State the blood parasite species.
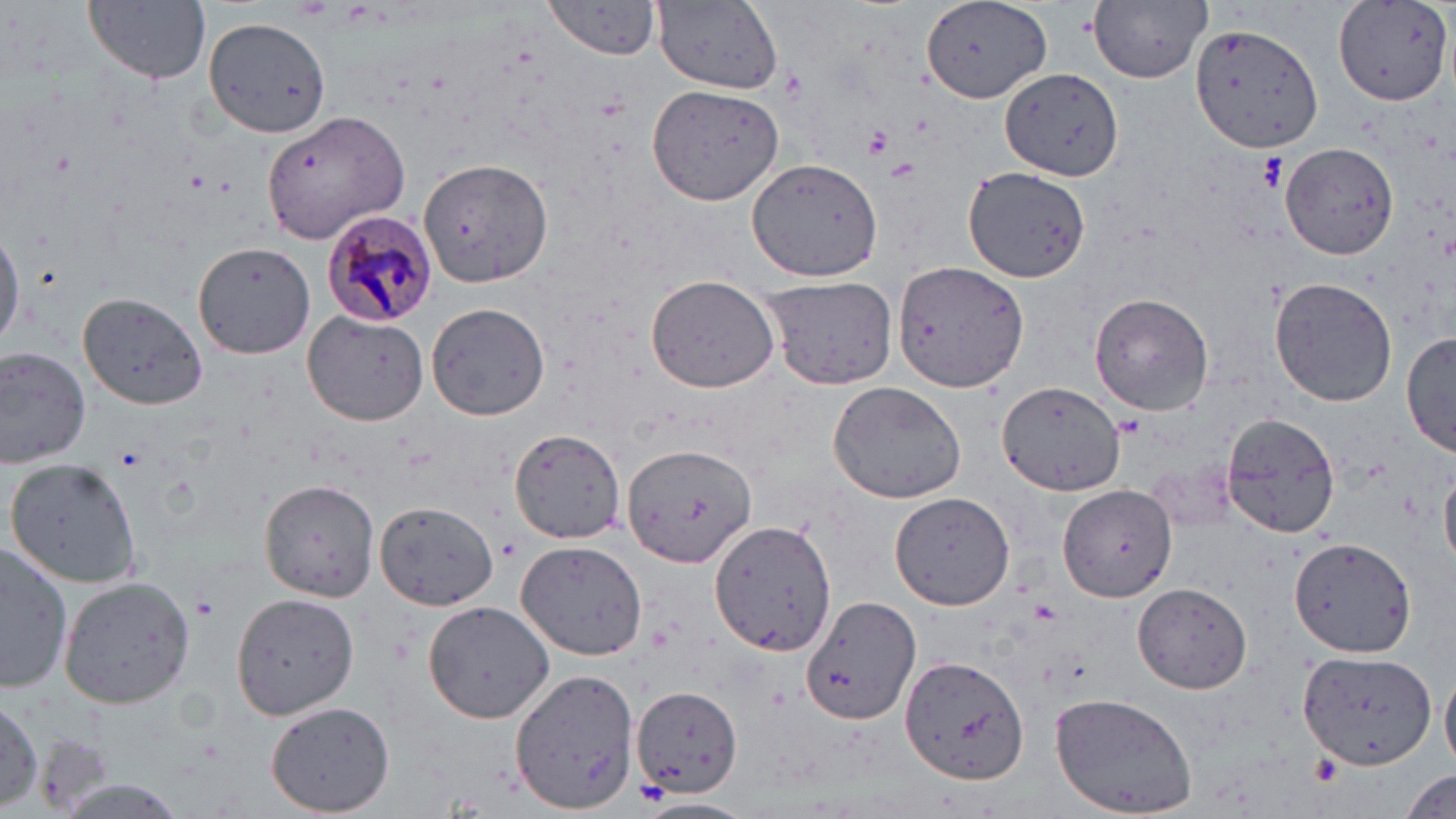
Plasmodium malariae.

Summary:
  - Coordinate format: approximate bounding boxes as (x1,y1)-(x2,y2) corner pairs in pixels
  - Platelet locations: (862,125)-(895,159), (1259,155)-(1285,190), (886,159)-(919,185), (114,445)-(148,472), (191,595)-(219,621)
  - Uninfected red blood cell locations: (544,0)-(665,59), (1089,0)-(1212,84), (84,1)-(209,84), (922,1)-(1054,105), (1333,1)-(1454,106), (654,2)-(783,91), (204,16)-(332,136), (1190,21)-(1323,155), (1000,67)-(1125,181), (648,84)-(785,206), (260,111)-(412,246), (1280,142)-(1397,258), (419,156)-(553,289), (747,156)-(885,282), (962,166)-(1090,282), (0,225)-(23,351), (193,240)-(316,358), (893,259)-(1031,392), (645,275)-(781,393), (759,277)-(899,389), (1270,277)-(1398,407), (79,291)-(209,410), (1090,293)-(1214,416), (426,301)-(549,423), (303,310)-(428,425), (1401,333)-(1455,458), (0,346)-(92,465), (828,380)-(970,504), (997,381)-(1124,496), (1222,412)-(1343,537), (511,429)-(625,543), (621,442)-(758,571), (5,457)-(147,590), (1442,469)-(1456,565), (260,477)-(380,602), (1056,486)-(1179,603), (890,492)-(1016,609), (369,505)-(496,616), (709,519)-(838,657), (1289,537)-(1417,658), (516,540)-(648,662), (2,543)-(74,693), (59,576)-(194,708), (1133,583)-(1251,692), (232,592)-(358,720), (802,593)-(920,727), (422,601)-(555,722), (1298,648)-(1437,770), (901,658)-(1029,785), (512,668)-(639,813), (1441,670)-(1456,773), (631,683)-(742,799), (1050,693)-(1199,817), (0,696)-(43,813), (265,701)-(394,817), (1401,769)-(1454,815), (55,780)-(192,817), (631,799)-(758,819)
  - Plasmodium malariae-infected red blood cell locations: (325,213)-(440,326)
  - Stain: May-Grünwald-Giemsa
  - Magnification: 1000x
  - Preparation: thin blood smear
  - Modality: optical microscopy
  - Image size: 1456×819 pixels
  - Field of view: single